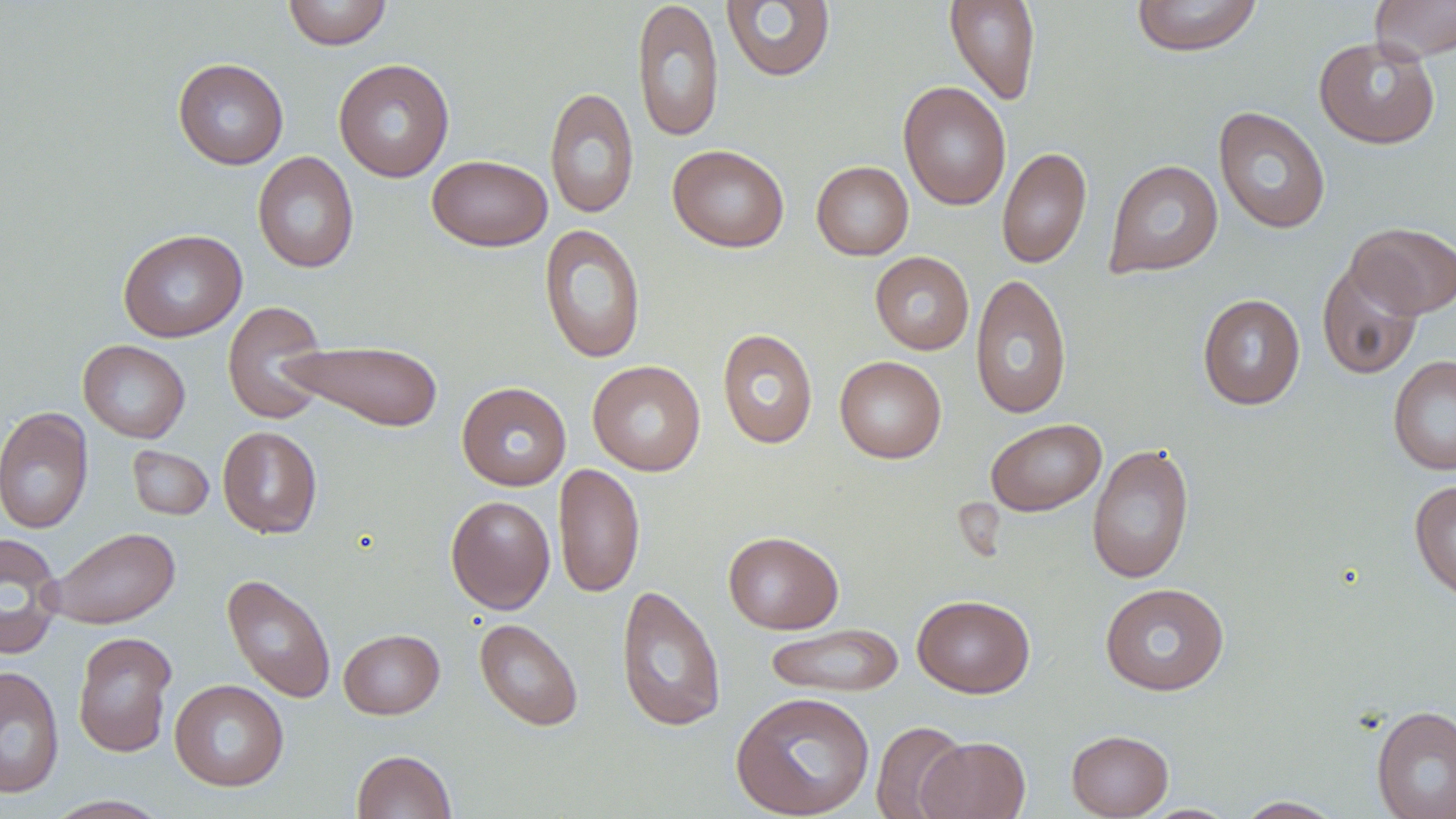

{
  "slide_level_diagnosis": "no evidence of blood parasites",
  "magnification": "1000x",
  "image_size": "1456×819 pixels",
  "modality": "light microscopy",
  "stain": "May-Grünwald-Giemsa",
  "field_of_view": "single",
  "preparation": "thin blood smear",
  "uninfected_red_blood_cell_locations": "approximate bounding boxes as [x1, y1, x2, y2] in pixels: [283, 0, 392, 50], [632, 0, 725, 142], [944, 0, 1041, 105], [1131, 0, 1262, 57], [1369, 0, 1456, 62], [720, 1, 836, 83], [1314, 36, 1441, 149], [173, 58, 288, 170], [333, 58, 455, 182], [898, 82, 1011, 211], [545, 86, 639, 220], [1213, 107, 1331, 234], [668, 144, 789, 252], [997, 147, 1091, 269], [252, 151, 359, 273], [426, 154, 552, 251], [1104, 159, 1223, 278], [811, 161, 913, 260], [1346, 222, 1456, 319], [539, 224, 646, 364], [118, 229, 247, 342], [869, 251, 974, 355], [1316, 260, 1423, 380], [970, 273, 1072, 420], [1197, 294, 1305, 410], [222, 301, 331, 425], [716, 328, 818, 449], [78, 339, 190, 443], [281, 339, 444, 432], [1388, 354, 1456, 476], [834, 356, 946, 463], [587, 360, 706, 477], [456, 381, 571, 490], [0, 406, 94, 534], [985, 418, 1107, 517], [217, 426, 322, 539], [1086, 442, 1195, 584], [127, 445, 214, 521], [553, 462, 645, 598], [1409, 479, 1456, 604], [445, 495, 556, 614], [45, 527, 181, 629], [723, 531, 844, 634], [0, 532, 65, 660], [222, 573, 337, 704], [1100, 582, 1229, 696], [615, 583, 727, 733], [912, 594, 1035, 698], [474, 618, 584, 731], [764, 623, 903, 698], [338, 628, 444, 719], [73, 631, 177, 757], [0, 666, 65, 798], [169, 679, 289, 791], [730, 690, 875, 819], [1371, 705, 1456, 819], [871, 720, 970, 819], [1066, 729, 1174, 818], [918, 736, 1030, 819], [351, 750, 457, 819], [45, 795, 171, 818], [1233, 796, 1344, 818], [1140, 803, 1240, 818]"
}